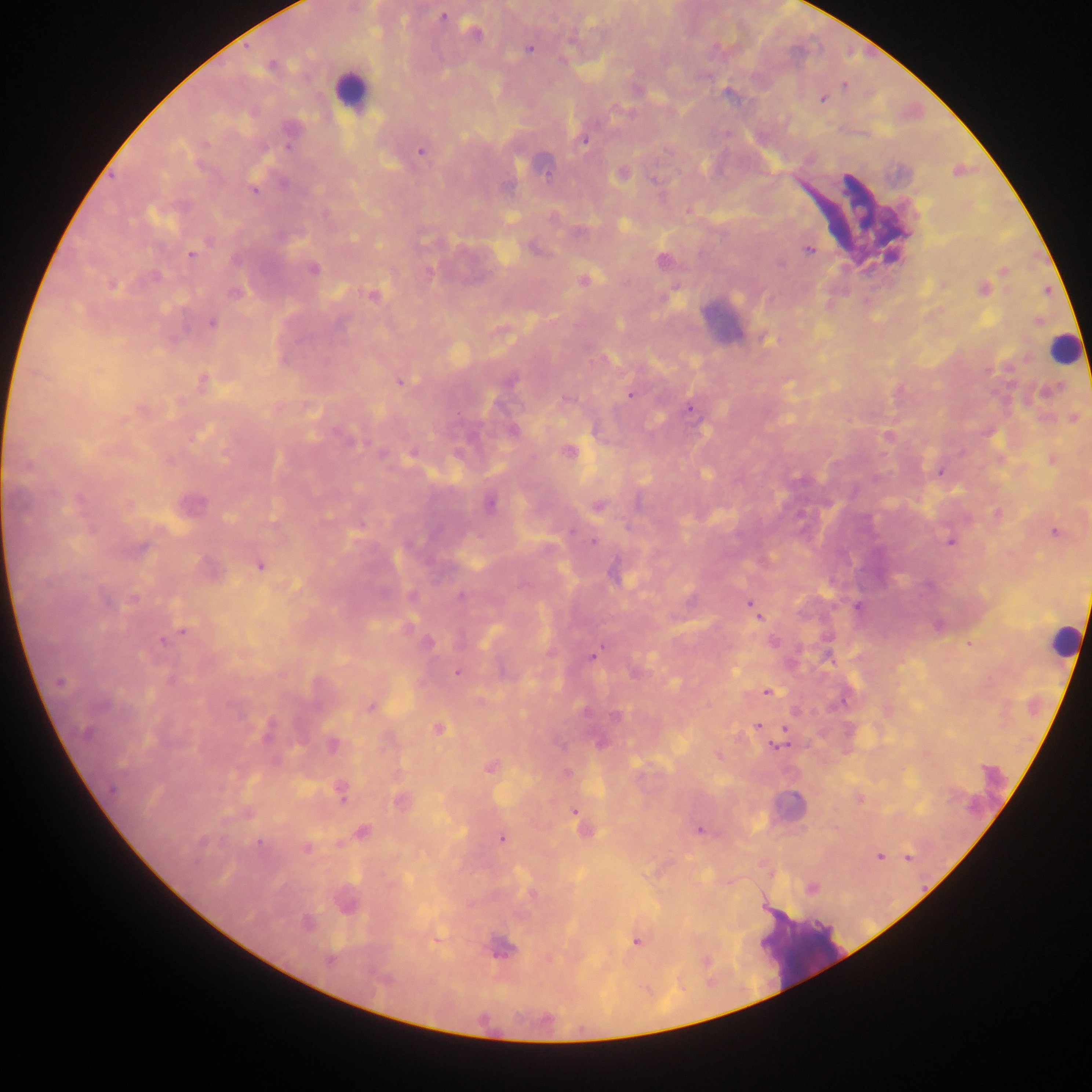 Approximate centers as {x, y} in pixels. Malaria parasite locations: {443, 17}, {475, 31}, {529, 49}, {270, 66}, {844, 84}, {822, 98}, {584, 140}, {420, 151}, {621, 174}, {254, 190}, {209, 241}, {809, 249}, {191, 254}, {235, 260}, {781, 264}, {313, 269}, {155, 278}, {583, 281}, {112, 285}, {983, 289}, {234, 293}, {373, 295}, {212, 323}, {767, 340}, {202, 382}, {401, 382}, {1048, 392}, {630, 395}, {565, 400}, {690, 410}, {1073, 418}, {513, 431}, {350, 440}, {568, 451}, {382, 454}, {412, 454}, {938, 472}, {705, 473}, {489, 505}, {598, 507}, {1055, 532}, {593, 541}, {950, 541}, {140, 548}, {260, 566}, {614, 575}, {459, 596}, {133, 599}, {750, 605}, {857, 607}, {756, 612}, {182, 631}, {162, 641}, {427, 642}, {773, 642}, {593, 655}, {457, 673}, {170, 680}, {60, 682}, {768, 692}, {371, 707}, {616, 717}, {757, 725}, {439, 729}, {85, 733}, {600, 743}, {332, 745}, {777, 746}, {491, 766}, {112, 789}, {342, 793}, {400, 801}, {573, 812}, {699, 831}, {362, 832}, {502, 839}, {202, 842}, {259, 842}, {307, 849}, {880, 856}, {908, 857}, {812, 888}, {346, 903}, {307, 923}, {637, 942}, {501, 949}, {329, 960}. Leukocyte locations: {350, 89}, {724, 320}, {1064, 348}, {1063, 639}, {784, 806}, {804, 951}. Image is 1092×1092 pixels. Collected in Ghana. Thick blood smear. One field of view. Photographed through a microscope with a mobile-phone camera.